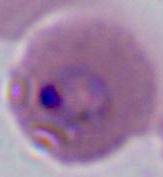

Summary:
  - Magnification: 400x or 1000x
  - Modality: micrograph
  - Identification: Plasmodium